State which parasite is depicted.
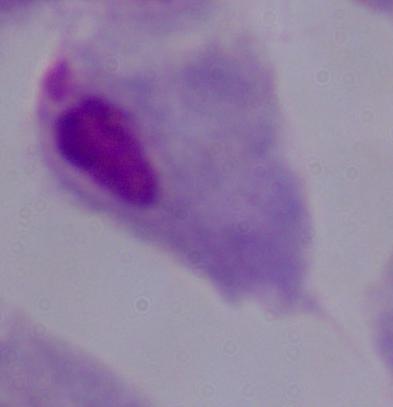

A trichomonad.

Micrograph. Captured at 1000x magnification.